Name the parasite shown.
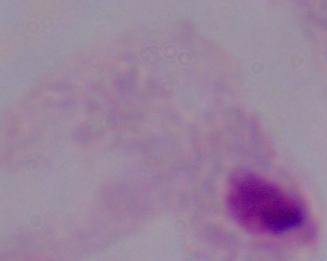
A trichomonad.

Captured at 1000x magnification. Photomicrograph.